Assess the morphology of the red blood cells.
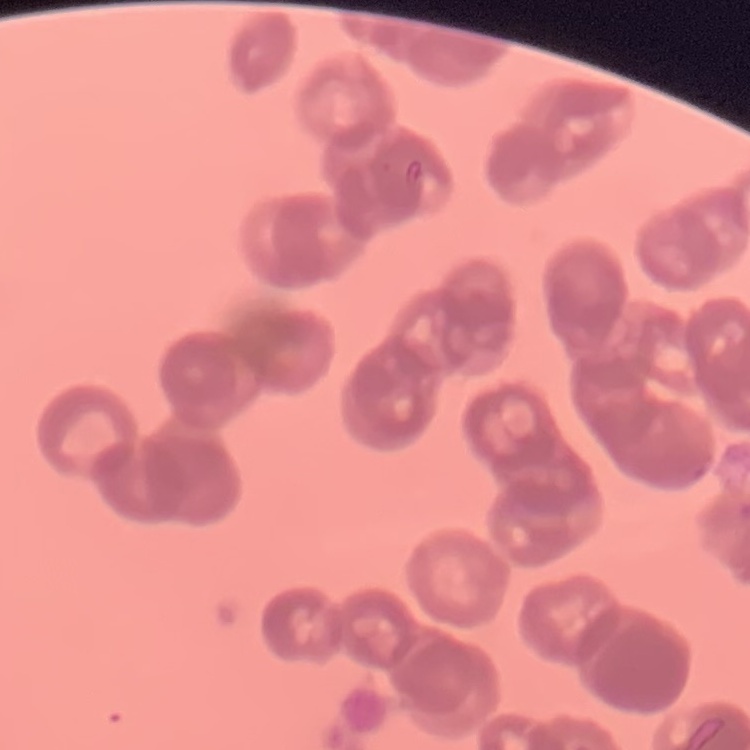

They show rouleaux formation.

{
  "stain": "Field's or Giemsa",
  "image_type": "square crop of a larger photomicrograph",
  "preparation": "thin blood film"
}